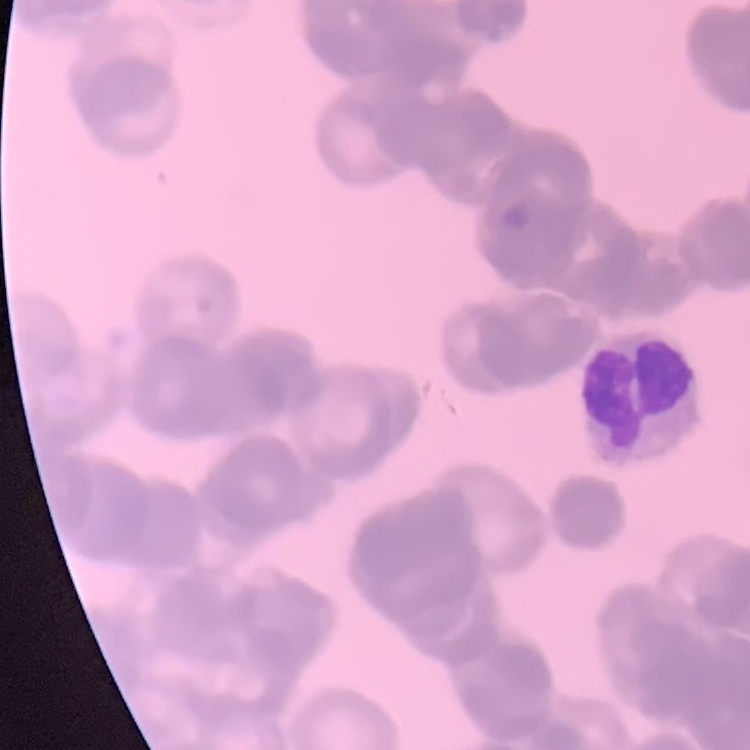

Summary:
  - Erythrocyte morphology: rouleaux formation
  - Preparation: thin peripheral smear
  - Stain: Field's or Giemsa
  - Image type: one tile cut from a larger photomicrograph